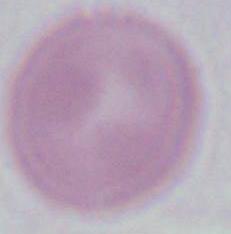
Summary:
  - Modality: micrograph
  - Identification: erythrocyte
  - Magnification: 1000x